Identify the parasite.
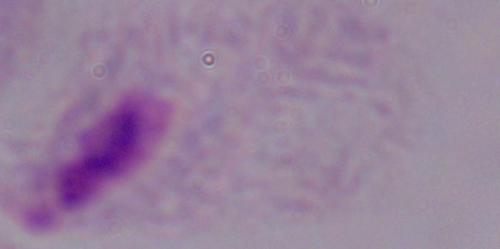

This is a trichomonad.

Summary:
  - Modality: photomicrograph
  - Magnification: 1000x